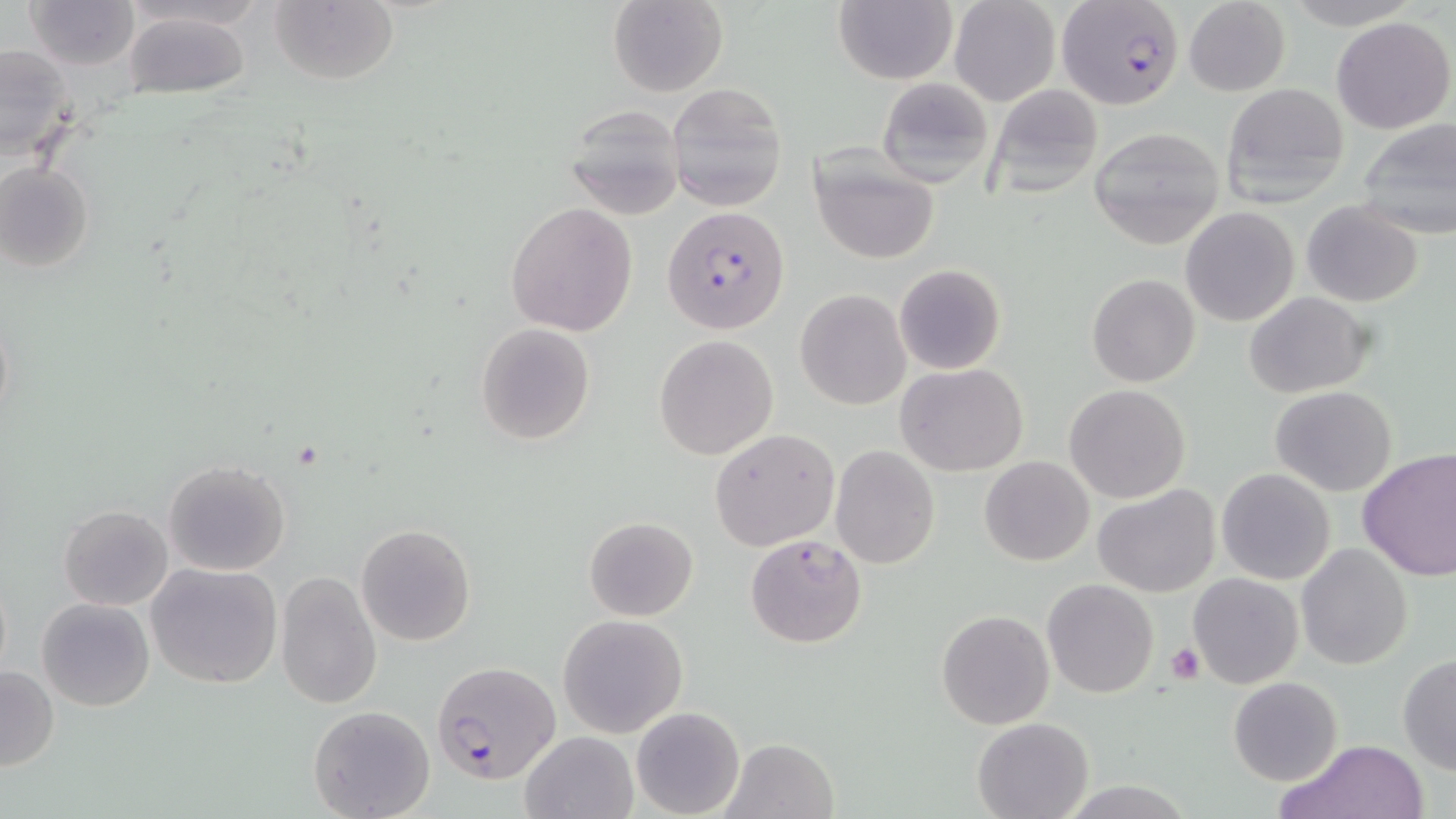
Summary:
  - Coordinate format: approximate bounding boxes as named x1/y1/x2/y2 corners in pixels
  - Uninfected red blood cell locations: (x1=25, y1=0, x2=140, y2=72), (x1=269, y1=0, x2=401, y2=86), (x1=608, y1=0, x2=728, y2=97), (x1=949, y1=0, x2=1061, y2=106), (x1=1183, y1=0, x2=1291, y2=96), (x1=832, y1=1, x2=957, y2=85), (x1=122, y1=11, x2=254, y2=101), (x1=1332, y1=16, x2=1453, y2=133), (x1=0, y1=44, x2=77, y2=160), (x1=876, y1=77, x2=992, y2=187), (x1=1220, y1=81, x2=1352, y2=206), (x1=666, y1=82, x2=789, y2=213), (x1=985, y1=84, x2=1103, y2=199), (x1=566, y1=107, x2=686, y2=219), (x1=1354, y1=117, x2=1456, y2=240), (x1=1089, y1=127, x2=1224, y2=249), (x1=809, y1=146, x2=940, y2=265), (x1=0, y1=162, x2=95, y2=272), (x1=1301, y1=200, x2=1423, y2=307), (x1=505, y1=202, x2=637, y2=336), (x1=1181, y1=206, x2=1299, y2=327), (x1=1127, y1=225, x2=1274, y2=354), (x1=894, y1=263, x2=1006, y2=375), (x1=1086, y1=274, x2=1200, y2=387), (x1=795, y1=289, x2=911, y2=410), (x1=1244, y1=291, x2=1374, y2=398), (x1=475, y1=323, x2=596, y2=444), (x1=653, y1=335, x2=779, y2=458), (x1=897, y1=362, x2=1027, y2=476), (x1=1062, y1=383, x2=1191, y2=503), (x1=1270, y1=386, x2=1396, y2=497), (x1=709, y1=428, x2=839, y2=550), (x1=831, y1=444, x2=940, y2=569), (x1=1357, y1=449, x2=1456, y2=581), (x1=979, y1=457, x2=1094, y2=567), (x1=163, y1=460, x2=292, y2=577), (x1=1216, y1=467, x2=1337, y2=585), (x1=1093, y1=485, x2=1221, y2=598), (x1=58, y1=504, x2=174, y2=610), (x1=584, y1=516, x2=698, y2=621), (x1=356, y1=524, x2=477, y2=646), (x1=746, y1=534, x2=867, y2=647), (x1=1296, y1=543, x2=1413, y2=669), (x1=144, y1=561, x2=283, y2=689), (x1=275, y1=571, x2=383, y2=710), (x1=1188, y1=573, x2=1306, y2=690), (x1=1042, y1=578, x2=1158, y2=698), (x1=36, y1=597, x2=155, y2=712), (x1=937, y1=609, x2=1054, y2=729), (x1=558, y1=613, x2=689, y2=738), (x1=1397, y1=653, x2=1456, y2=774), (x1=1, y1=665, x2=59, y2=772), (x1=1230, y1=676, x2=1342, y2=784), (x1=308, y1=704, x2=436, y2=819), (x1=630, y1=705, x2=745, y2=818), (x1=972, y1=717, x2=1093, y2=819), (x1=519, y1=731, x2=638, y2=819), (x1=723, y1=737, x2=839, y2=819), (x1=1283, y1=738, x2=1429, y2=819)
  - Platelet locations: (x1=1168, y1=642, x2=1203, y2=684)
  - Plasmodium falciparum-infected red blood cell locations: (x1=1054, y1=0, x2=1184, y2=110), (x1=662, y1=206, x2=790, y2=334), (x1=429, y1=664, x2=558, y2=789)
  - Slide-level diagnosis: Plasmodium falciparum
  - Image size: 1456×819 pixels
  - Stain: May-Grünwald-Giemsa
  - Field of view: single
  - Preparation: thin blood smear
  - Magnification: 1000x
  - Modality: optical microscopy